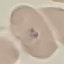

{
  "result": "no malaria parasites detected",
  "image_type": "automatically extracted cell patch, resized to 64 × 64 pixels",
  "capture": "smartphone through the microscope eyepiece",
  "stain": "Giemsa",
  "preparation": "thin blood smear"
}